Describe the morphology of the erythrocytes.
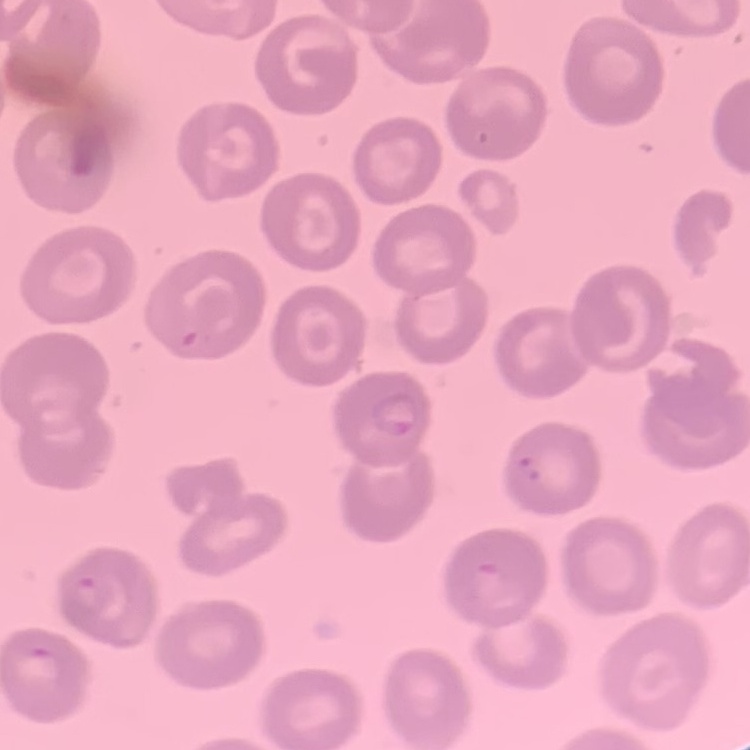
They show no rouleaux formation.

Thin blood film. Stained with either Field's or Giemsa. One tile cut from a larger photomicrograph.